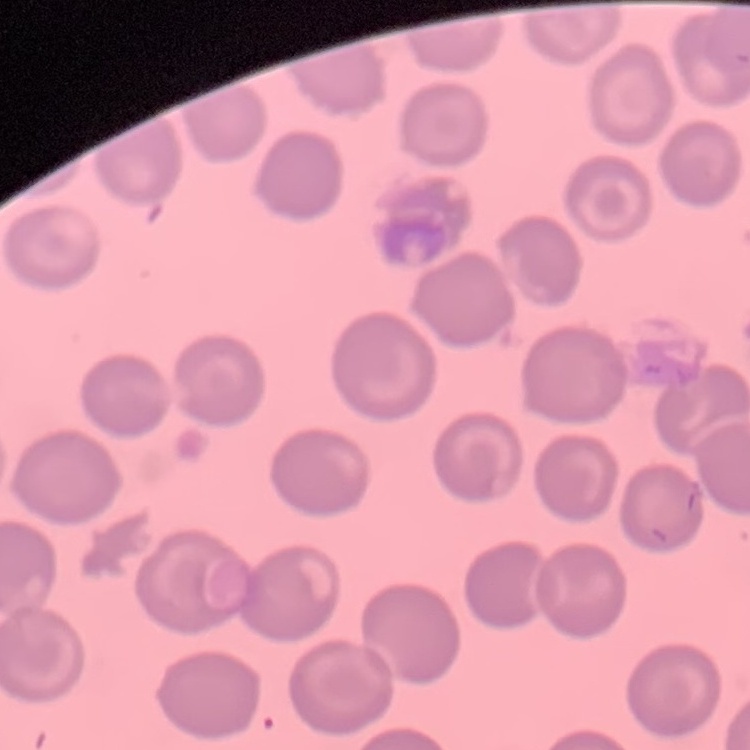

Summary:
  - Red blood cell morphology: no rouleaux formation
  - Stain: Field's or Giemsa
  - Image type: one tile cut from a larger photomicrograph
  - Preparation: thin peripheral smear